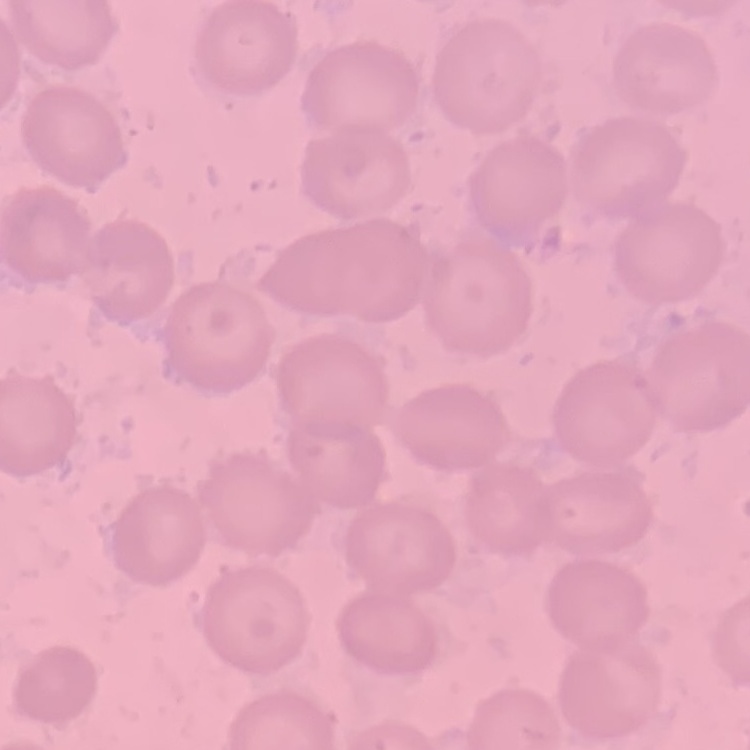
erythrocyte morphology = no rouleaux formation
preparation = thin peripheral smear
stain = Field's or Giemsa
image type = square crop of a larger photomicrograph